Outline each uninfected red blood cell.
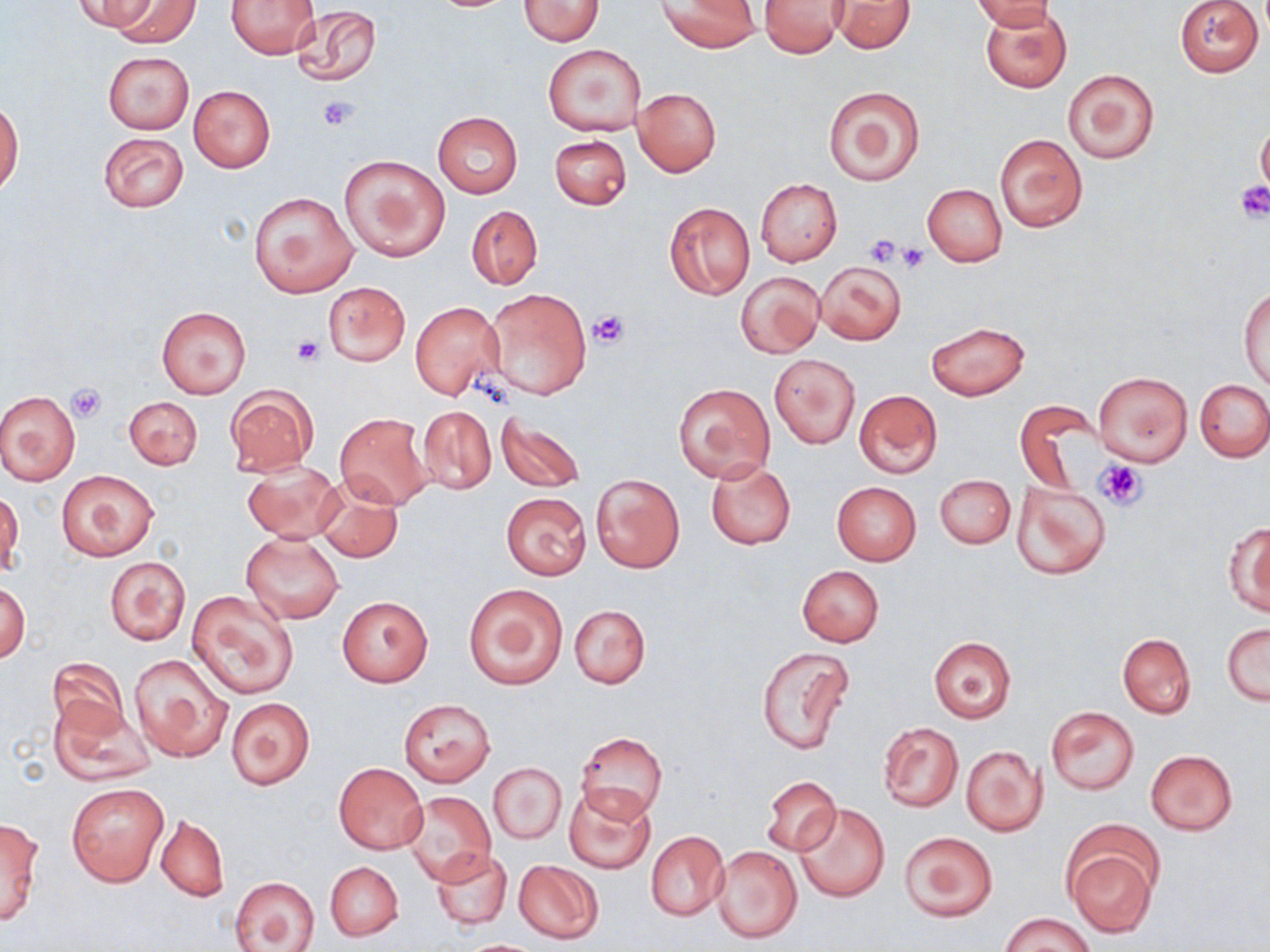
Approximate bounding boxes as [x1, y1, x2, y2] in pixels.
Uninfected red blood cells: [72, 0, 158, 32], [106, 0, 199, 45], [518, 0, 604, 45], [658, 0, 760, 52], [831, 0, 916, 53], [970, 0, 1058, 30], [1175, 0, 1263, 77], [228, 1, 320, 59], [759, 1, 846, 57], [290, 5, 381, 89], [979, 5, 1073, 93], [542, 44, 646, 136], [102, 52, 193, 134], [1062, 68, 1159, 164], [823, 84, 926, 187], [188, 85, 276, 172], [633, 87, 721, 176], [0, 101, 22, 194], [432, 112, 522, 198], [1257, 118, 1270, 201], [98, 131, 189, 213], [993, 132, 1089, 232], [550, 134, 632, 209], [339, 155, 450, 261], [756, 179, 842, 266], [922, 184, 1007, 266], [250, 190, 359, 298], [664, 201, 754, 299], [466, 205, 543, 289], [815, 260, 906, 344], [736, 272, 824, 358], [323, 280, 409, 367], [1240, 287, 1269, 390], [483, 288, 592, 400], [410, 301, 505, 398], [157, 306, 250, 398], [926, 321, 1029, 400], [769, 353, 859, 448], [1093, 369, 1193, 467], [1196, 379, 1270, 462], [673, 383, 775, 482], [226, 385, 317, 476], [854, 390, 942, 478], [0, 391, 80, 485], [124, 396, 202, 470], [1014, 402, 1099, 496], [417, 405, 496, 494], [495, 411, 585, 495], [334, 413, 433, 509], [242, 459, 343, 544], [706, 460, 796, 549], [57, 468, 157, 561], [592, 473, 684, 573], [935, 474, 1015, 548], [313, 477, 406, 565], [1011, 478, 1111, 580], [832, 481, 921, 565], [0, 490, 23, 579], [501, 492, 591, 579], [1225, 522, 1270, 616], [241, 530, 346, 623], [104, 556, 190, 645], [796, 566, 885, 646], [1, 581, 30, 664], [463, 582, 568, 689], [187, 590, 300, 700], [337, 595, 433, 687], [569, 604, 651, 689], [1222, 623, 1269, 704], [1117, 633, 1196, 718], [929, 637, 1016, 722], [756, 645, 856, 753], [128, 653, 233, 761], [46, 657, 130, 741], [48, 695, 154, 787], [226, 697, 315, 789], [399, 699, 495, 786], [1045, 706, 1140, 795], [877, 722, 963, 812], [576, 731, 667, 820], [961, 746, 1047, 836], [1146, 750, 1238, 835], [335, 763, 427, 853], [488, 763, 567, 845], [762, 776, 840, 856], [67, 782, 168, 887], [563, 783, 656, 873], [402, 791, 496, 887], [794, 803, 890, 902], [156, 815, 229, 901], [0, 816, 45, 925], [645, 831, 728, 921], [899, 831, 997, 923], [1066, 843, 1158, 937], [710, 844, 804, 944], [432, 849, 510, 928], [513, 860, 603, 944], [325, 861, 403, 941], [231, 875, 321, 951], [1002, 913, 1093, 952], [461, 939, 547, 951].

slide-level diagnosis = negative for blood parasites
magnification = 1000x
modality = optical microscopy
stain = May-Grünwald-Giemsa
preparation = thin blood film
image size = 1270×952 pixels
platelet locations = approximate bounding boxes as [x1, y1, x2, y2] in pixels: [318, 97, 360, 131], [1235, 181, 1270, 222], [865, 234, 902, 266], [898, 245, 930, 273], [587, 308, 631, 348], [292, 337, 322, 366], [66, 385, 107, 422], [1096, 459, 1148, 510]
field of view = single